Outline each uninfected red blood cell.
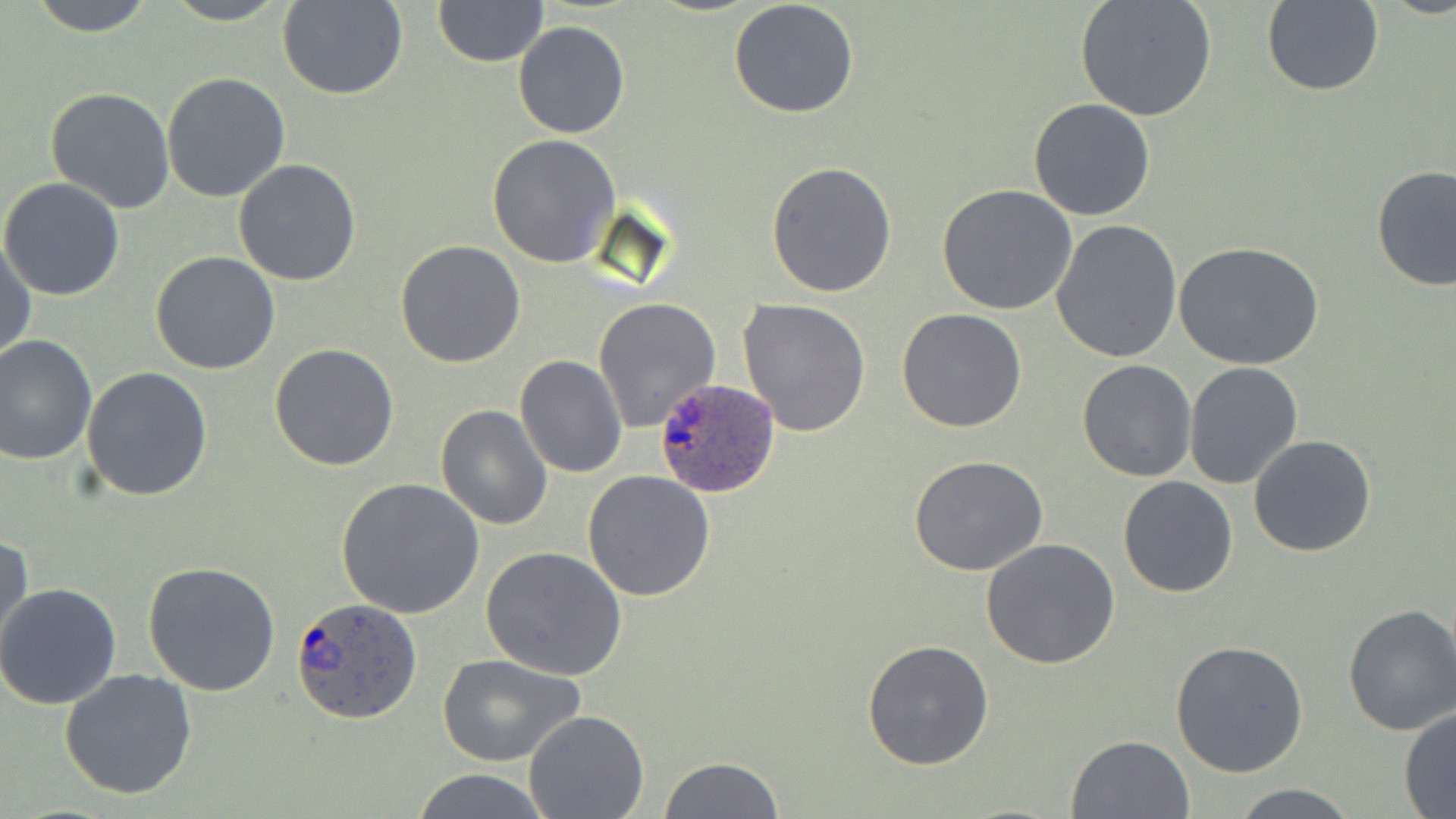
Approximate bounding boxes as (x1,y1)-(x2,y2) corner pairs in pixels.
Uninfected red blood cells: (28,0)-(158,37), (160,0)-(290,26), (278,0)-(406,100), (431,0)-(546,67), (728,0)-(860,118), (1075,0)-(1218,122), (1262,1)-(1382,97), (512,21)-(630,139), (161,73)-(290,205), (45,87)-(177,213), (1028,98)-(1157,221), (488,134)-(622,267), (232,158)-(363,286), (766,162)-(897,298), (1371,164)-(1455,293), (0,178)-(126,301), (937,185)-(1078,316), (1052,220)-(1184,362), (0,237)-(36,364), (394,240)-(525,368), (1174,242)-(1325,371), (149,252)-(280,375), (593,298)-(723,434), (737,298)-(872,436), (896,308)-(1027,432), (0,335)-(98,466), (269,342)-(400,470), (514,355)-(628,478), (1077,359)-(1196,481), (1184,361)-(1304,489), (82,367)-(214,502), (436,404)-(554,531), (1249,434)-(1376,558), (909,456)-(1048,576), (583,469)-(716,601), (1118,476)-(1238,597), (336,477)-(484,619), (1,527)-(33,659), (981,538)-(1120,670), (481,547)-(628,682), (141,561)-(281,697), (0,582)-(122,710), (1340,602)-(1456,737), (863,637)-(996,771), (1170,638)-(1312,778), (435,652)-(585,767), (58,667)-(198,799), (1399,707)-(1456,816), (523,710)-(650,819), (1066,733)-(1195,819), (659,757)-(786,818), (408,770)-(552,819), (1229,781)-(1361,818).

Summary:
  - Plasmodium ovale-infected red blood cell locations: (654,373)-(777,499), (291,595)-(422,723)
  - Slide-level diagnosis: Plasmodium ovale
  - Stain: May-Grünwald-Giemsa
  - Magnification: 1000x
  - Preparation: thin blood smear
  - Field of view: one of a larger specimen
  - Modality: optical microscopy
  - Image size: 1456×819 pixels